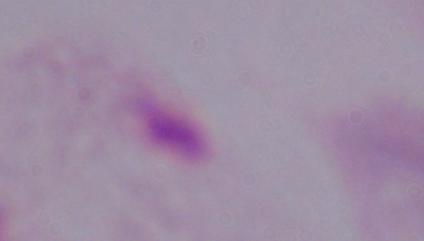

Summary:
  - Identification: trichomonad
  - Modality: micrograph
  - Magnification: 1000x